Give the position of every leukocyte visible.
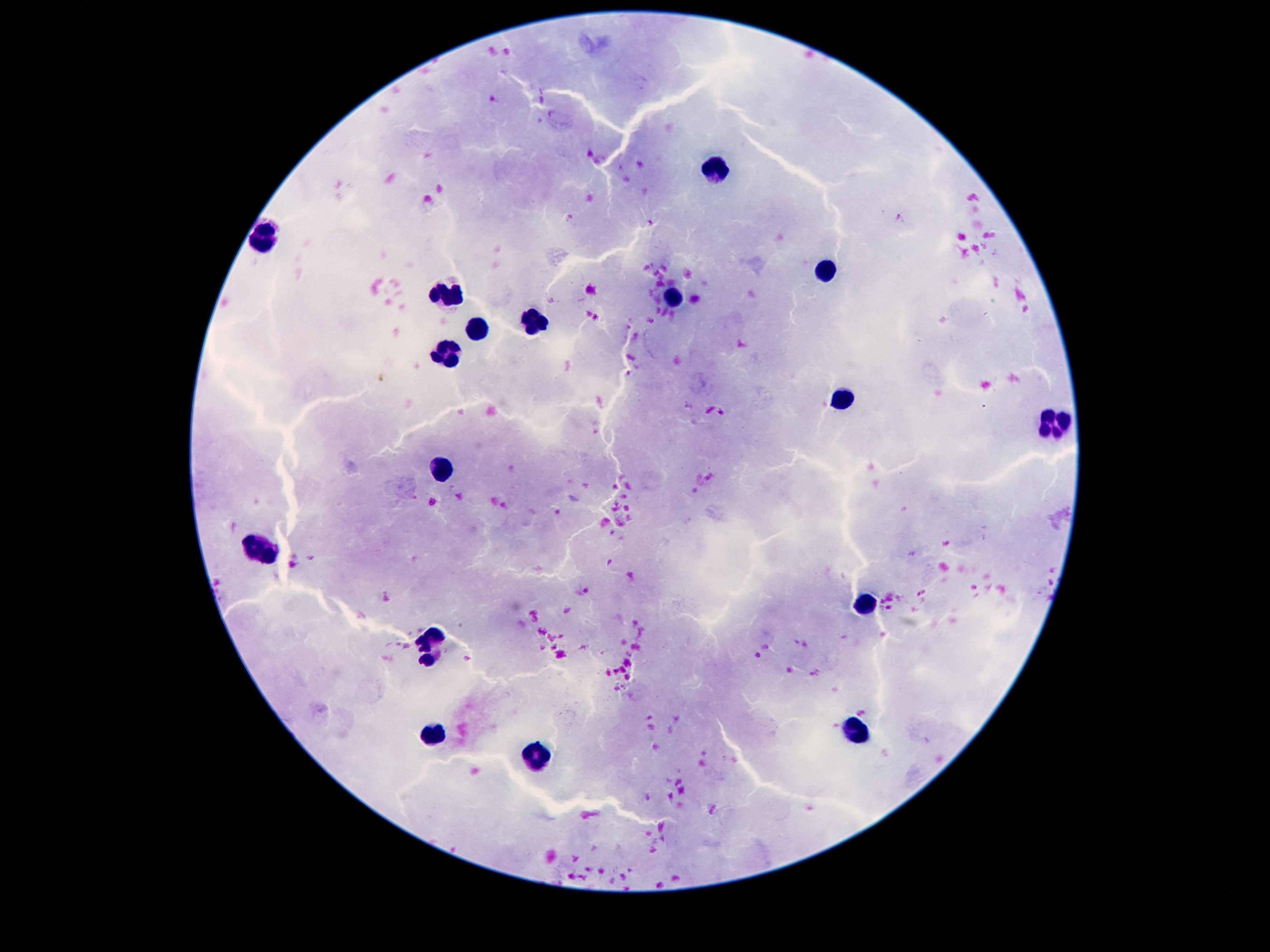

Approximate object centers, in pixels from the top-left corner.
Leukocytes: (x=713, y=168), (x=262, y=239), (x=827, y=267), (x=451, y=295), (x=673, y=299), (x=539, y=318), (x=474, y=325), (x=445, y=355), (x=842, y=398), (x=1056, y=426), (x=442, y=466), (x=262, y=547), (x=863, y=602), (x=430, y=642), (x=854, y=732), (x=434, y=738), (x=537, y=757).

Summary:
  - Magnification: 100x
  - Image size: 1270×952 pixels
  - Field of view: one from this slide
  - Patient malaria status: uninfected
  - Preparation: thick peripheral-blood smear
  - Stain: Giemsa
  - Capture: smartphone camera through the microscope eyepiece